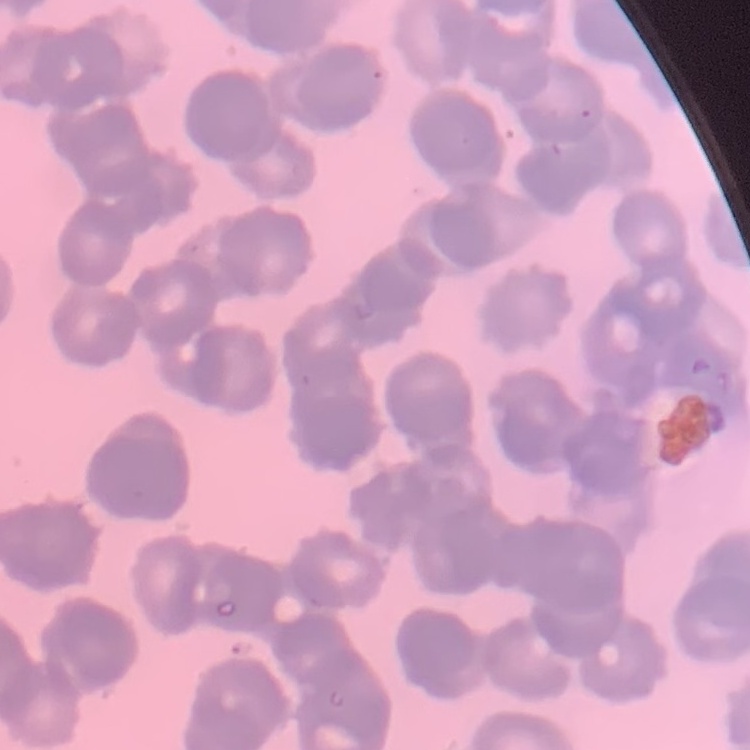
Summary:
  - Red blood cell morphology: rouleaux formation
  - Image type: square crop of a larger photomicrograph
  - Preparation: thin peripheral smear
  - Stain: Field's or Giemsa